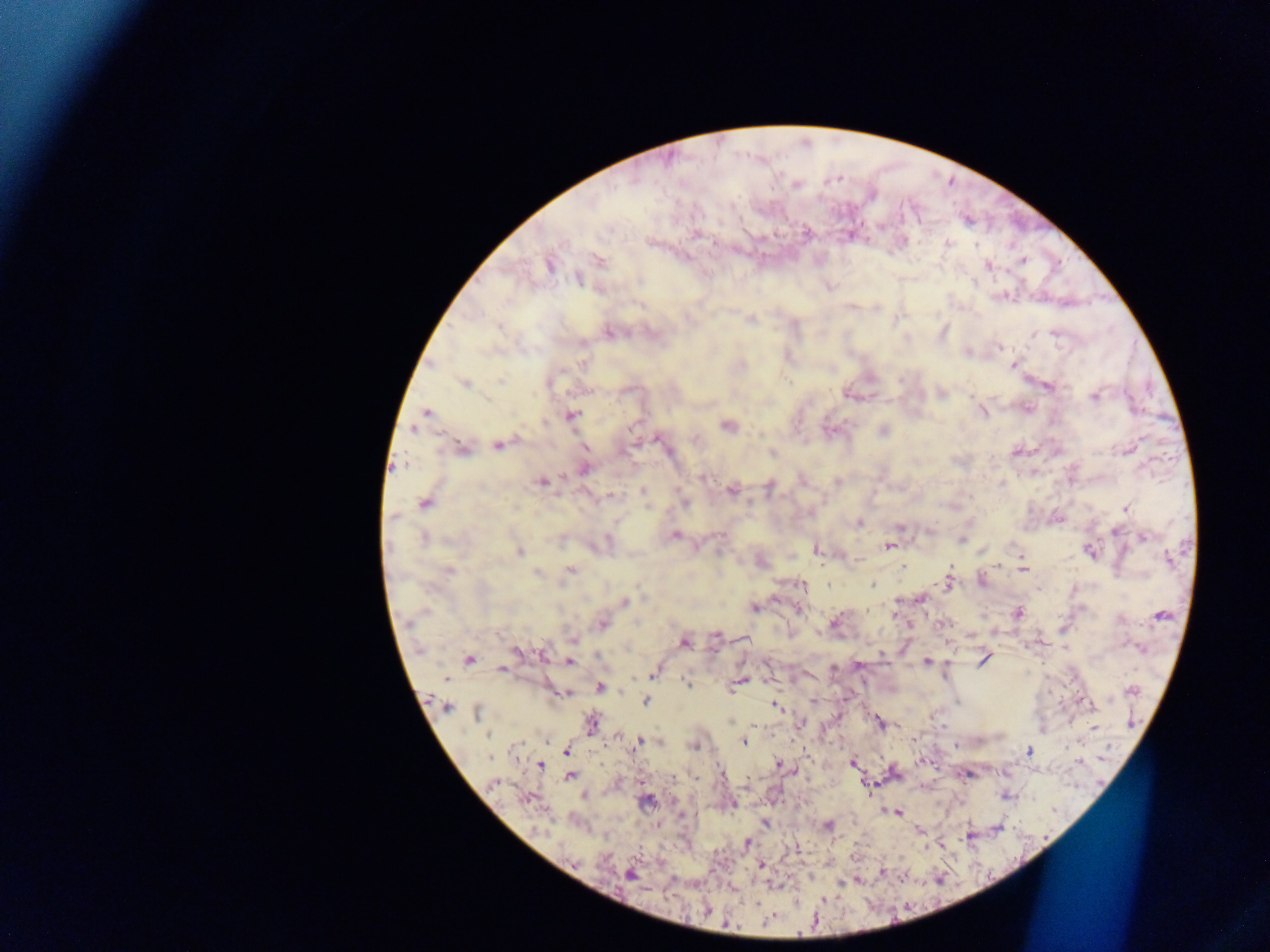

Approximate centers as [x, y] in pixels. Malaria parasite locations: [695, 235], [947, 243], [1022, 260], [600, 261], [549, 265], [987, 265], [579, 278], [751, 319], [500, 327], [608, 333], [1056, 334], [1033, 335], [999, 347], [742, 365], [1013, 366], [500, 380], [464, 382], [1049, 386], [1094, 397], [1028, 409], [427, 412], [983, 412], [570, 415], [545, 422], [727, 426], [631, 428], [412, 429], [884, 430], [658, 439], [498, 445], [585, 447], [463, 449], [772, 454], [584, 469], [703, 477], [837, 481], [542, 482], [769, 488], [732, 490], [642, 491], [611, 497], [425, 503], [685, 503], [1125, 508], [393, 517], [859, 523], [900, 526], [1115, 532], [675, 536], [1144, 537], [424, 538], [961, 540], [888, 546], [817, 549], [1090, 551], [519, 552], [1169, 559], [999, 565], [903, 566], [1022, 569], [570, 570], [448, 571], [537, 573], [981, 581], [948, 584], [802, 585], [872, 585], [828, 586], [921, 598], [625, 601], [754, 607], [798, 609], [1017, 612], [894, 615], [1161, 615], [835, 620], [602, 624], [715, 635], [573, 639], [684, 643], [515, 651], [543, 653], [469, 659], [984, 659], [569, 661], [927, 661], [501, 668], [653, 672], [740, 681], [686, 682], [600, 687], [1132, 690], [564, 694], [646, 701], [1088, 703], [446, 705], [775, 706], [476, 713], [592, 723], [1094, 727], [489, 735], [638, 742], [743, 743], [693, 746], [566, 751], [1029, 751], [490, 758], [852, 762], [779, 764], [540, 766], [570, 776], [673, 778], [696, 778], [494, 783], [647, 801], [732, 805], [898, 812], [765, 823], [828, 826], [747, 842], [761, 865], [629, 874], [757, 903], [767, 921], [726, 924]. Thick blood film. Image is 1270×952 pixels. Sample from Ghana. One field of view. Mobile-phone photograph taken through the microscope.